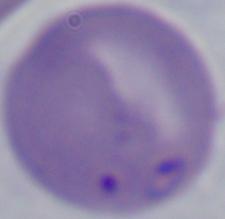
identification = Babesia
magnification = 1000x
modality = micrograph